Locate every blood parasite and identify its species.
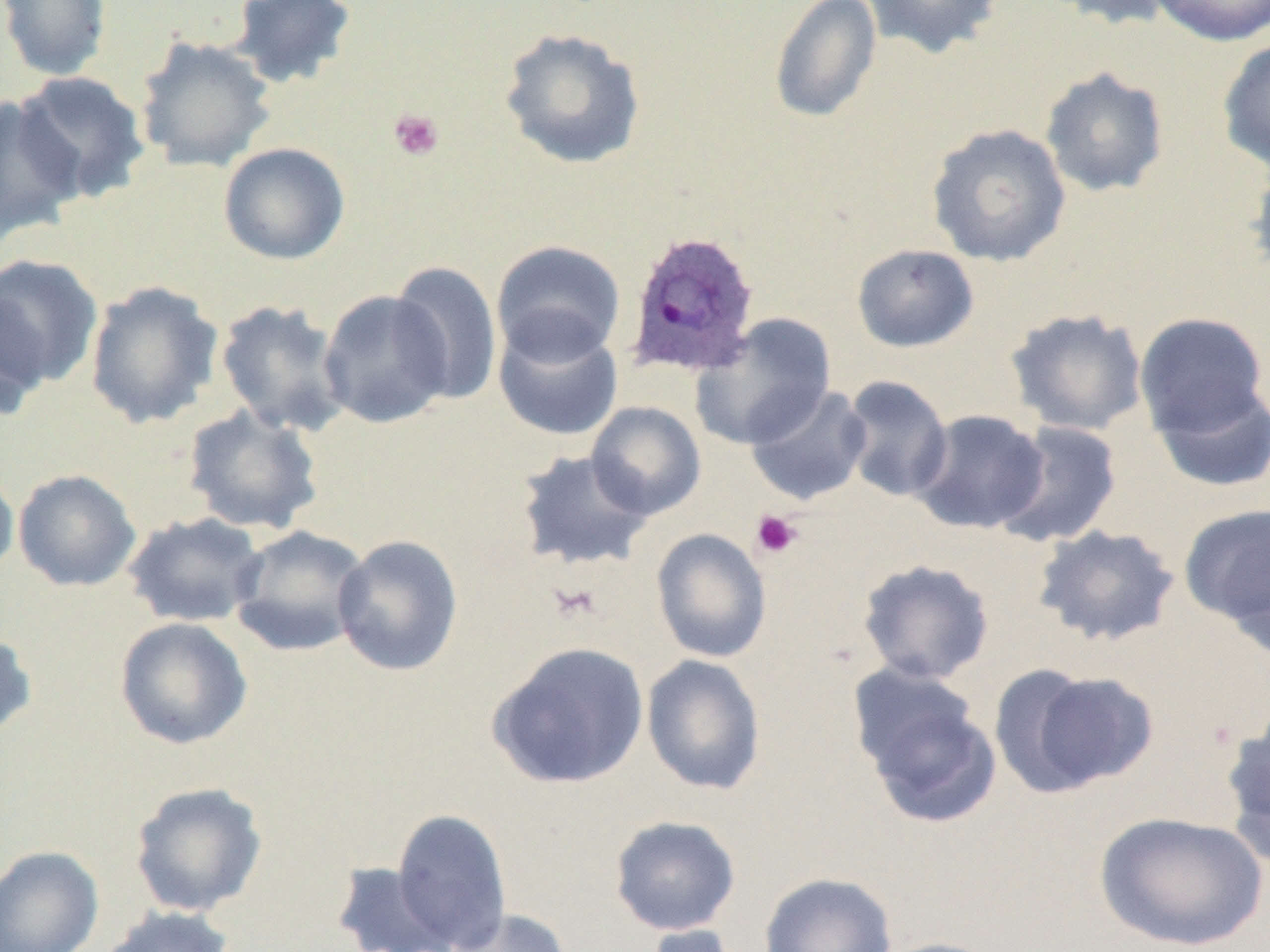
Approximate bounding boxes as (x1, y1, x2, y2) in pixels.
Plasmodium ovale-infected red blood cells: (623, 229, 761, 379).
No Plasmodium falciparum, Plasmodium malariae, Plasmodium vivax, Babesia divergens, or Trypanosoma brucei observed.

slide_level_diagnosis: Plasmodium ovale
platelet_locations: 'approximate bounding boxes as (x1, y1, x2, y2) in pixels: (388, 108, 444, 162), (751, 510, 803, 559), (547, 580, 603, 624)'
magnification: 1000x
modality: optical microscopy
field_of_view: one of a larger specimen
preparation: thin blood smear
uninfected_red_blood_cell_locations: 'approximate bounding boxes as (x1, y1, x2, y2) in pixels: (0, 0, 114, 82), (862, 0, 1005, 59), (1043, 0, 1182, 30), (1147, 0, 1270, 47), (227, 1, 358, 89), (768, 1, 882, 124), (498, 27, 647, 171), (134, 35, 277, 174), (1217, 37, 1270, 175), (1040, 66, 1170, 198), (11, 71, 150, 205), (0, 95, 84, 244), (926, 123, 1071, 267), (218, 142, 350, 265), (1246, 156, 1270, 285), (490, 240, 626, 365), (851, 243, 979, 353), (0, 254, 104, 392), (389, 261, 503, 405), (84, 280, 224, 428), (318, 289, 454, 428), (0, 292, 51, 422), (214, 299, 352, 437), (1005, 308, 1149, 437), (1134, 312, 1269, 438), (690, 314, 836, 450), (493, 316, 624, 442), (840, 375, 954, 503), (1150, 380, 1270, 493), (745, 383, 873, 506), (586, 401, 706, 520), (182, 404, 325, 536), (910, 409, 1049, 535), (994, 421, 1123, 548), (514, 448, 654, 572), (0, 464, 19, 582), (13, 469, 142, 592), (1179, 503, 1269, 637), (122, 512, 268, 628), (228, 525, 371, 657), (1032, 525, 1181, 647), (651, 528, 772, 663), (332, 534, 464, 677), (857, 559, 994, 684), (114, 617, 253, 750), (0, 628, 38, 741), (487, 641, 650, 790), (641, 654, 766, 795), (1002, 668, 1158, 794), (852, 679, 1002, 828), (1219, 709, 1270, 865), (129, 781, 268, 917), (392, 808, 512, 950), (1094, 810, 1268, 951), (609, 815, 741, 936), (0, 845, 104, 952), (330, 861, 459, 952), (759, 872, 897, 952), (96, 905, 238, 952), (444, 907, 572, 952), (640, 922, 748, 952), (872, 937, 1007, 952)'
image_size: 1270×952 pixels